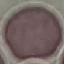

Summary:
  - Result: no malaria parasites seen
  - Stain: Giemsa
  - Preparation: thin blood smear
  - Image type: automatically extracted cell patch, resized to 64 × 64 pixels
  - Capture: smartphone through the microscope eyepiece